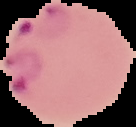
result = malaria parasites detected
preparation = thin blood smear
image type = segmented cell region with the area outside set to black
image size = 136×127 pixels